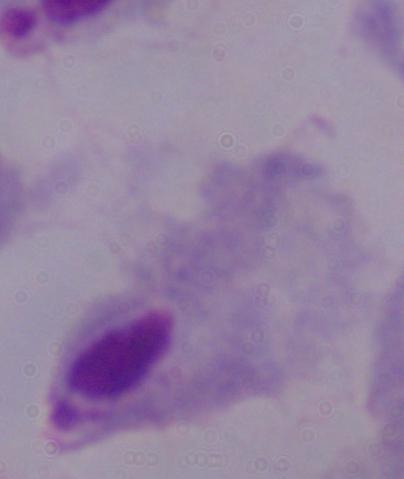

A trichomonad is shown. Micrograph. Captured at 1000x magnification.